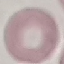
Result: no malaria parasites seen. Photographed with a smartphone camera at the microscope eyepiece. Cell patch, automatically extracted from a larger field of view and resized to 64 × 64 pixels. Thin smear of blood. Giemsa stain.